Outline each Plasmodium falciparum-infected red blood cell.
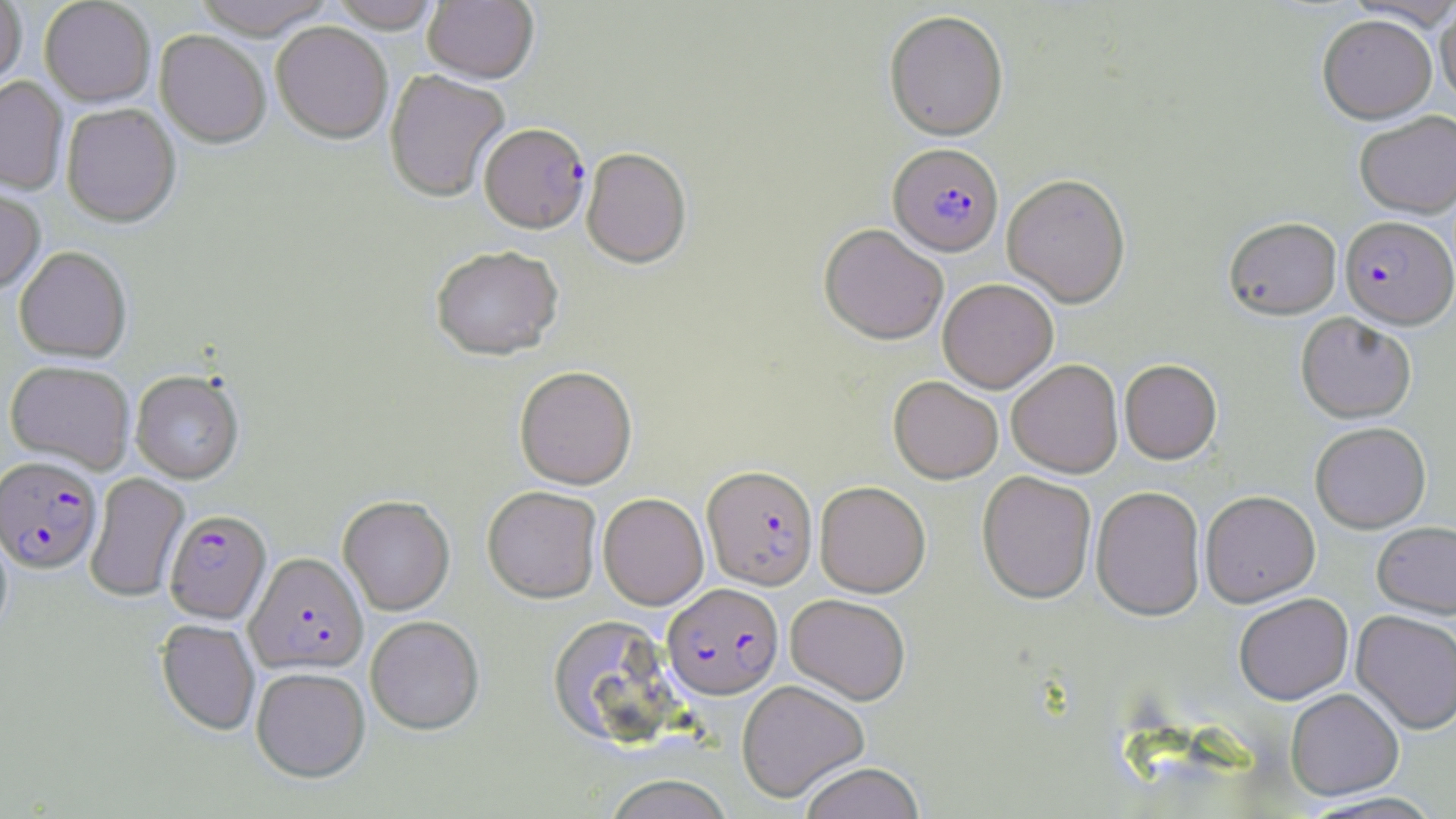

Approximate bounding boxes as named x1/y1/x2/y2 corners in pixels.
Plasmodium falciparum-infected red blood cells: (x1=479, y1=123, x2=591, y2=234), (x1=888, y1=143, x2=1003, y2=256), (x1=1340, y1=216, x2=1456, y2=329), (x1=0, y1=456, x2=103, y2=575), (x1=702, y1=464, x2=818, y2=589), (x1=164, y1=510, x2=271, y2=624), (x1=246, y1=552, x2=368, y2=674), (x1=662, y1=583, x2=783, y2=698).

Uninfected red blood cell locations: (x1=0, y1=0, x2=27, y2=94), (x1=39, y1=0, x2=155, y2=108), (x1=193, y1=0, x2=336, y2=40), (x1=329, y1=0, x2=441, y2=34), (x1=423, y1=0, x2=539, y2=86), (x1=1435, y1=2, x2=1456, y2=106), (x1=884, y1=10, x2=1009, y2=141), (x1=1318, y1=14, x2=1437, y2=123), (x1=271, y1=23, x2=393, y2=145), (x1=154, y1=31, x2=271, y2=149), (x1=384, y1=70, x2=510, y2=203), (x1=0, y1=78, x2=68, y2=195), (x1=61, y1=104, x2=180, y2=229), (x1=1355, y1=110, x2=1456, y2=218), (x1=581, y1=148, x2=692, y2=269), (x1=1002, y1=173, x2=1131, y2=307), (x1=0, y1=188, x2=46, y2=297), (x1=1224, y1=216, x2=1341, y2=319), (x1=819, y1=223, x2=949, y2=344), (x1=430, y1=245, x2=564, y2=361), (x1=14, y1=247, x2=132, y2=363), (x1=938, y1=278, x2=1058, y2=393), (x1=1296, y1=312, x2=1416, y2=423), (x1=1007, y1=359, x2=1123, y2=477), (x1=1119, y1=359, x2=1222, y2=463), (x1=4, y1=360, x2=135, y2=474), (x1=514, y1=366, x2=637, y2=489), (x1=131, y1=370, x2=244, y2=483), (x1=889, y1=375, x2=1003, y2=483), (x1=1310, y1=421, x2=1431, y2=533), (x1=976, y1=470, x2=1096, y2=604), (x1=84, y1=473, x2=190, y2=603), (x1=815, y1=480, x2=931, y2=597), (x1=482, y1=485, x2=602, y2=603), (x1=1091, y1=485, x2=1206, y2=620), (x1=1200, y1=490, x2=1320, y2=606), (x1=598, y1=493, x2=709, y2=610), (x1=338, y1=495, x2=455, y2=616), (x1=1372, y1=520, x2=1456, y2=617), (x1=0, y1=526, x2=13, y2=641), (x1=785, y1=593, x2=911, y2=704), (x1=1234, y1=593, x2=1353, y2=704), (x1=1351, y1=609, x2=1456, y2=733), (x1=547, y1=614, x2=682, y2=748), (x1=365, y1=615, x2=485, y2=735), (x1=156, y1=619, x2=260, y2=736), (x1=251, y1=666, x2=370, y2=782), (x1=736, y1=679, x2=869, y2=802), (x1=1285, y1=688, x2=1404, y2=799), (x1=798, y1=762, x2=925, y2=819), (x1=603, y1=775, x2=735, y2=819), (x1=1298, y1=791, x2=1447, y2=818). Slide-level diagnosis: Plasmodium falciparum. Thin blood smear. Light microscopy. May-Grünwald-Giemsa stain. Image is 1456×819 pixels. Single field of view. Captured at 1000x magnification.